State which cell type is depicted.
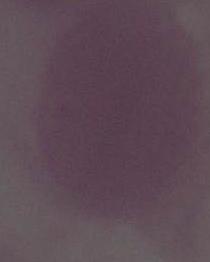
This is an erythrocyte.

Summary:
  - Modality: micrograph
  - Magnification: 1000x